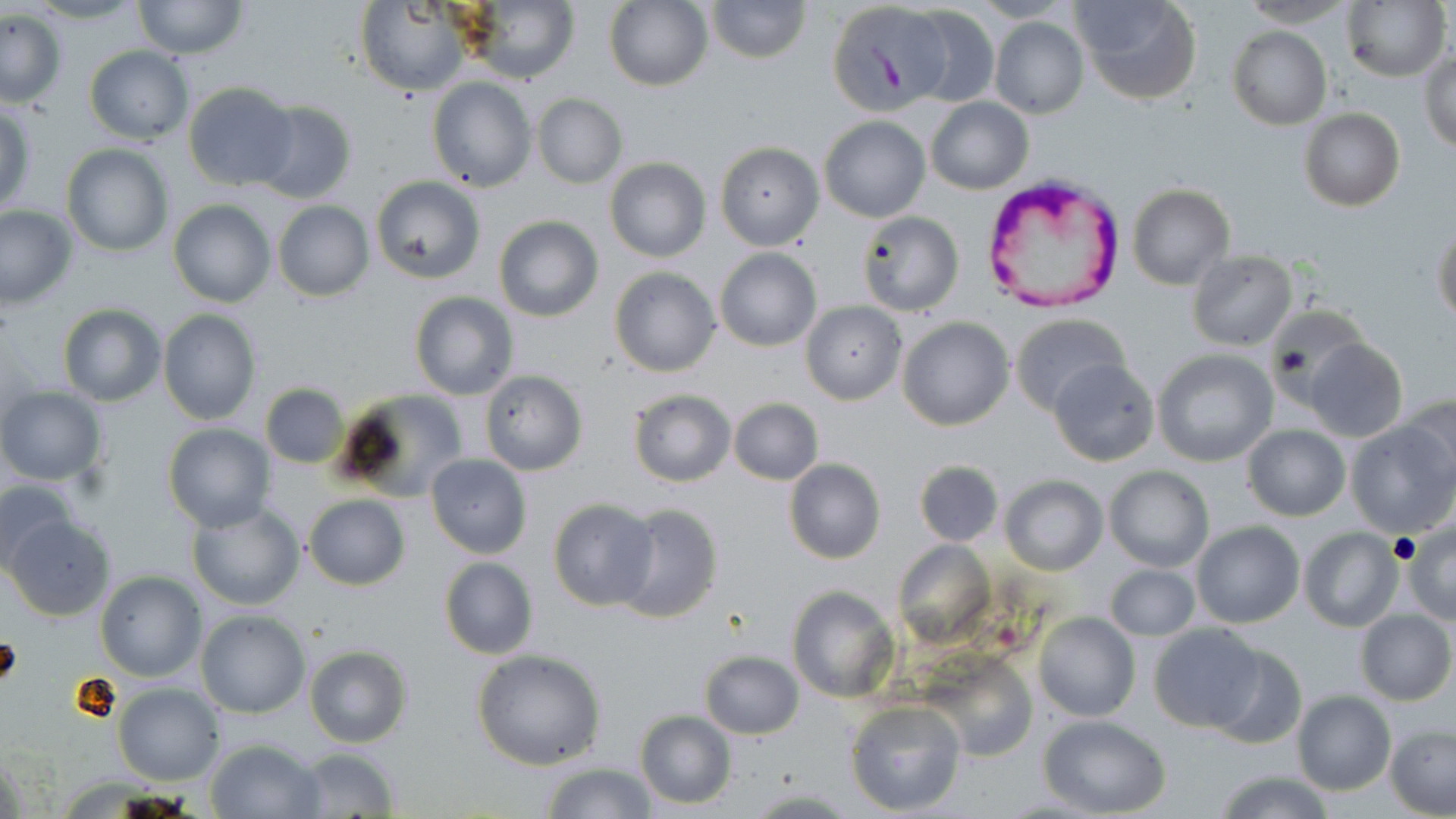

{
  "slide_level_diagnosis": "Plasmodium vivax",
  "stain": "May-Grünwald-Giemsa",
  "preparation": "thin blood film",
  "uninfected_red_blood_cell_locations": "approximate bounding boxes as [x1, y1, x2, y2] in pixels: [707, 0, 810, 63], [1073, 0, 1202, 105], [1238, 0, 1354, 27], [1343, 0, 1449, 83], [132, 1, 248, 61], [605, 1, 712, 91], [826, 2, 948, 114], [356, 3, 470, 95], [459, 3, 578, 83], [904, 4, 999, 109], [1, 9, 66, 108], [990, 16, 1089, 119], [1227, 26, 1331, 129], [82, 46, 194, 145], [1419, 48, 1456, 154], [427, 77, 535, 191], [184, 83, 297, 191], [532, 94, 626, 188], [926, 97, 1032, 194], [250, 100, 357, 204], [0, 101, 35, 221], [1298, 109, 1405, 210], [819, 116, 930, 222], [715, 141, 824, 251], [61, 143, 174, 258], [605, 158, 710, 262], [371, 176, 486, 285], [1127, 183, 1235, 290], [169, 200, 275, 308], [272, 201, 373, 302], [0, 204, 77, 308], [857, 211, 964, 318], [494, 215, 602, 322], [1433, 223, 1456, 329], [714, 248, 821, 351], [1187, 251, 1298, 351], [609, 267, 720, 376], [409, 291, 519, 399], [801, 302, 906, 405], [57, 304, 166, 407], [1265, 308, 1366, 397], [157, 310, 261, 425], [1010, 313, 1128, 417], [898, 317, 1014, 431], [1303, 338, 1408, 441], [1151, 349, 1278, 468], [1048, 358, 1159, 467], [480, 372, 586, 475], [260, 383, 348, 469], [0, 387, 106, 486], [335, 389, 469, 502], [627, 389, 736, 487], [1398, 393, 1456, 490], [728, 398, 823, 484], [1347, 421, 1452, 538], [161, 424, 275, 533], [1221, 424, 1334, 606], [1241, 425, 1351, 522], [426, 455, 531, 558], [784, 459, 885, 565], [915, 460, 1004, 547], [1104, 466, 1214, 571], [1001, 475, 1107, 575], [0, 480, 79, 575], [302, 493, 410, 591], [548, 499, 658, 610], [609, 502, 724, 624], [186, 503, 306, 611], [5, 515, 117, 620], [1192, 521, 1304, 628], [1405, 521, 1456, 622], [1299, 527, 1404, 632], [894, 538, 995, 652], [439, 557, 539, 659], [1104, 564, 1200, 641], [96, 570, 206, 681], [787, 584, 899, 704], [196, 609, 311, 718], [1355, 610, 1455, 705], [1033, 612, 1141, 723], [1149, 623, 1264, 732], [1206, 643, 1306, 748], [303, 645, 413, 748], [472, 648, 607, 770], [699, 650, 804, 739], [932, 657, 1036, 761], [114, 682, 224, 785], [1291, 691, 1395, 795], [845, 700, 966, 816], [635, 711, 736, 808], [1039, 716, 1170, 817], [1385, 725, 1455, 817], [206, 739, 324, 817], [294, 747, 398, 818], [539, 762, 656, 818], [1215, 770, 1334, 819], [744, 788, 856, 817]",
  "field_of_view": "single",
  "modality": "optical microscopy",
  "magnification": "1000x",
  "image_size": "1456×819 pixels",
  "plasmodium_vivax_infected_red_blood_cell_locations": "approximate bounding boxes as [x1, y1, x2, y2] in pixels: [985, 171, 1124, 310]"
}